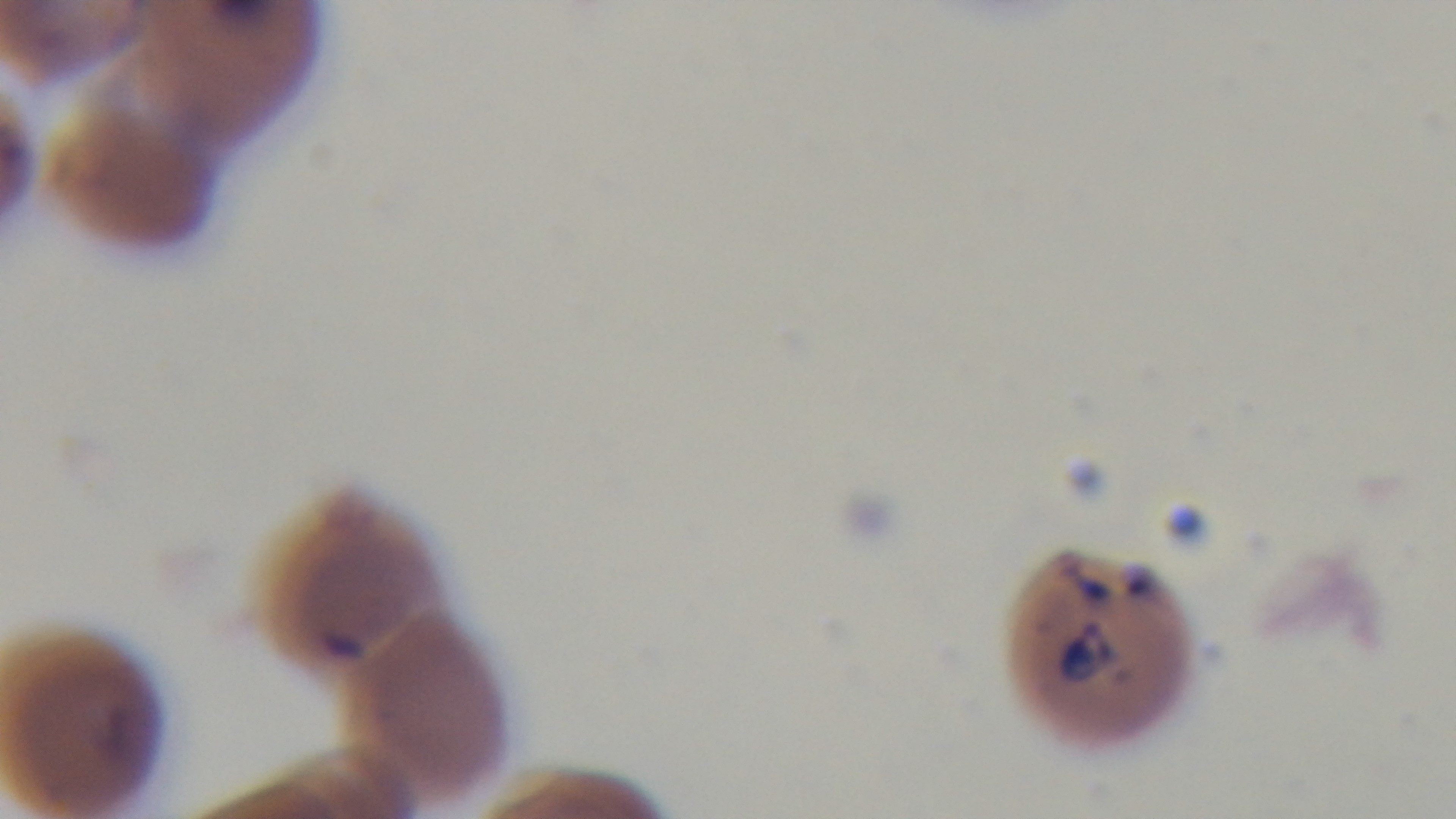

malaria status = positive
modality = light microscopy
preparation = thin smear
objective = 100x oil immersion
field of view = one from the slide
stain = Giemsa
capture = mounted 4K digital camera